Point out each malaria parasite.
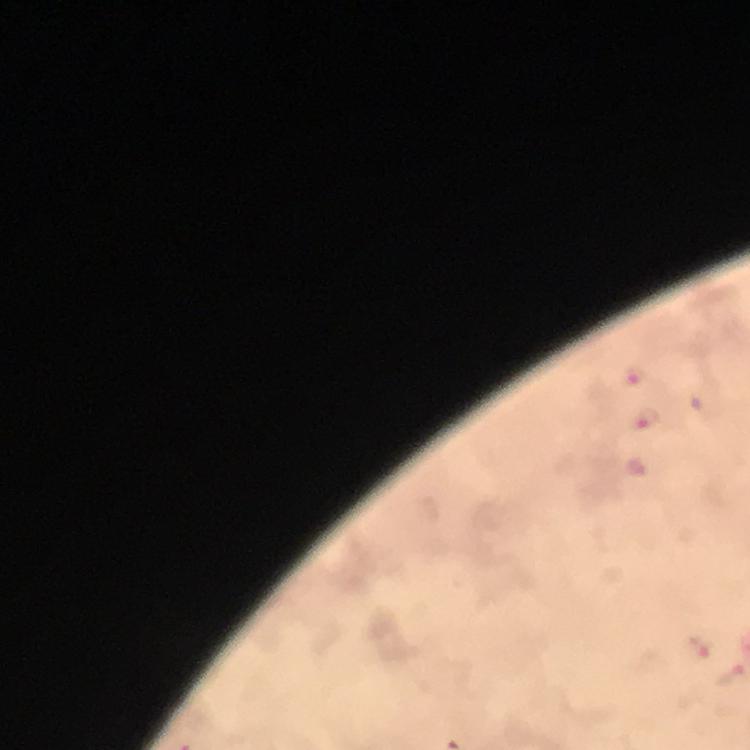
Approximate object centers, in pixels from the top-left corner.
Malaria parasites: (x=635, y=377), (x=650, y=420).

From a diagnostic examination for malaria. Giemsa-stained preparation. At 100x magnification. Image is 750×750 pixels. Photographed through the microscope with a smartphone camera. Immersion oil was used. A crop from one field of view. Thick blood film.